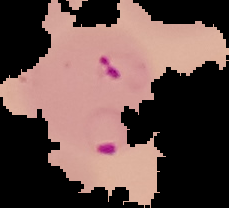
Segmented cell region on a black background. From a thin blood smear. Result: malaria parasites detected. Image is 229×208 pixels.